Describe the morphology of the red blood cells.
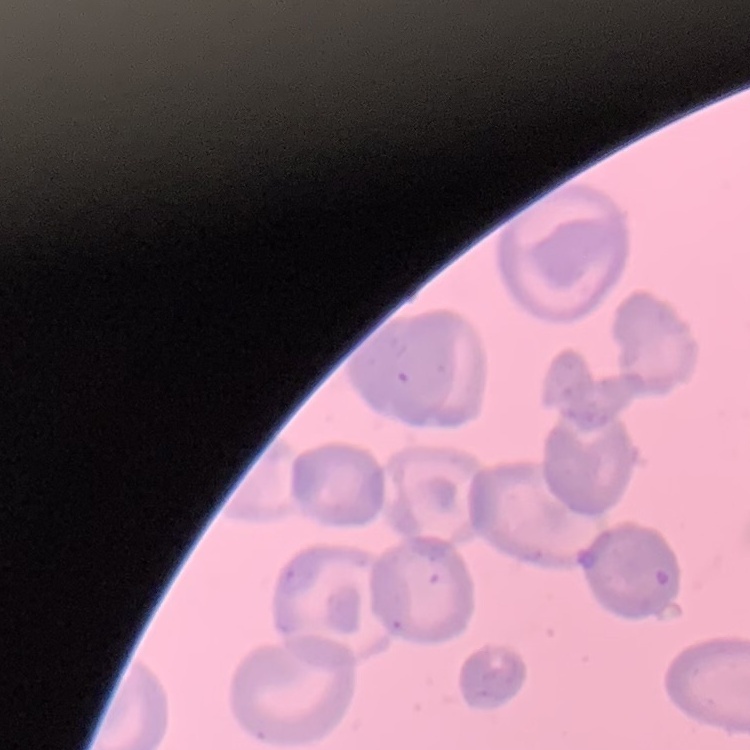
No rouleaux formation.

Stained with either Field's or Giemsa. Square crop of a larger photomicrograph. Thin blood film.